Comment on the morphology of the red blood cells.
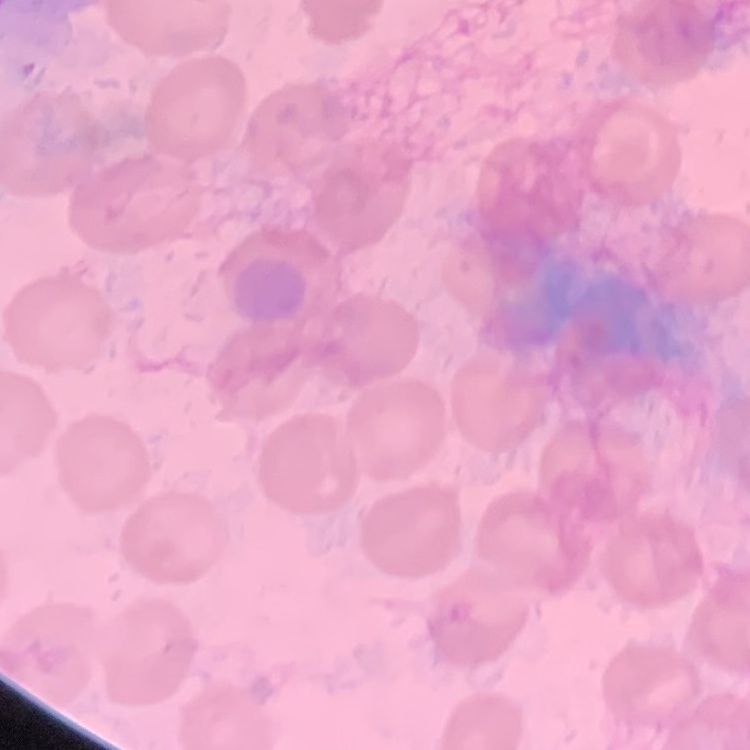
They show no rouleaux formation.

Summary:
  - Image type: one tile cut from a larger photomicrograph
  - Stain: Field's or Giemsa
  - Preparation: thin peripheral smear